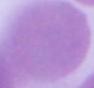
Summary:
  - Magnification: 1000x
  - Identification: red blood cell
  - Modality: photomicrograph